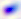 Micrograph. 400x magnification. Toxoplasma gondii is seen.